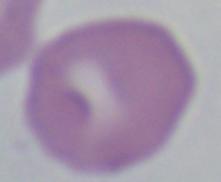

Summary:
  - Magnification: 1000x
  - Identification: Babesia
  - Modality: photomicrograph